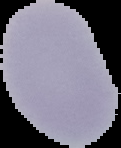 Image is 121×148 pixels. Malaria status: uninfected. From a thin blood film. Segmented cell region on a black background.